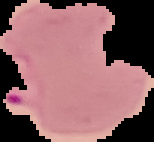
{
  "image_type": "segmented cell region with the area outside set to black",
  "image_size": "154×142 pixels",
  "result": "Plasmodium parasites detected",
  "preparation": "thin blood film"
}